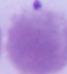 Photomicrograph. An erythrocyte is seen. 1000x magnification.